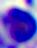
{
  "modality": "photomicrograph",
  "identification": "leukocyte",
  "magnification": "400x"
}